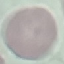
Malaria status: uninfected. Thin blood smear. Giemsa stain. Cell patch, automatically extracted from a larger field of view and resized to 64 × 64 pixels. Acquired by smartphone through the microscope eyepiece.